Name the parasite shown.
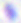

This is Toxoplasma gondii.

modality = photomicrograph
magnification = 400x